State which cell type is depicted.
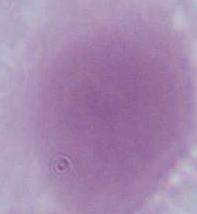

An erythrocyte.

{
  "modality": "photomicrograph",
  "magnification": "1000x"
}